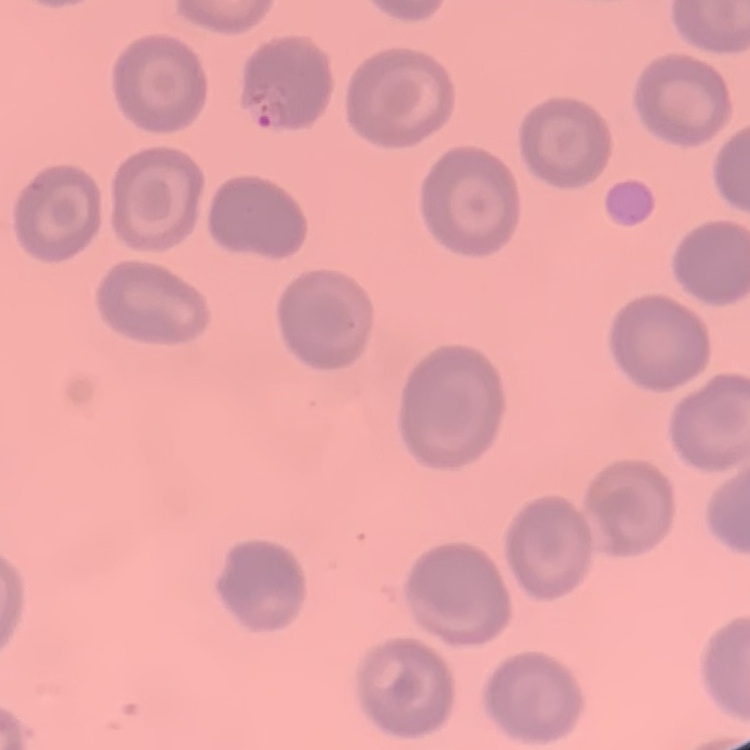

The red blood cells show no rouleaux formation. Thin blood film. One tile cut from a larger photomicrograph. Stained with either Field's or Giemsa.